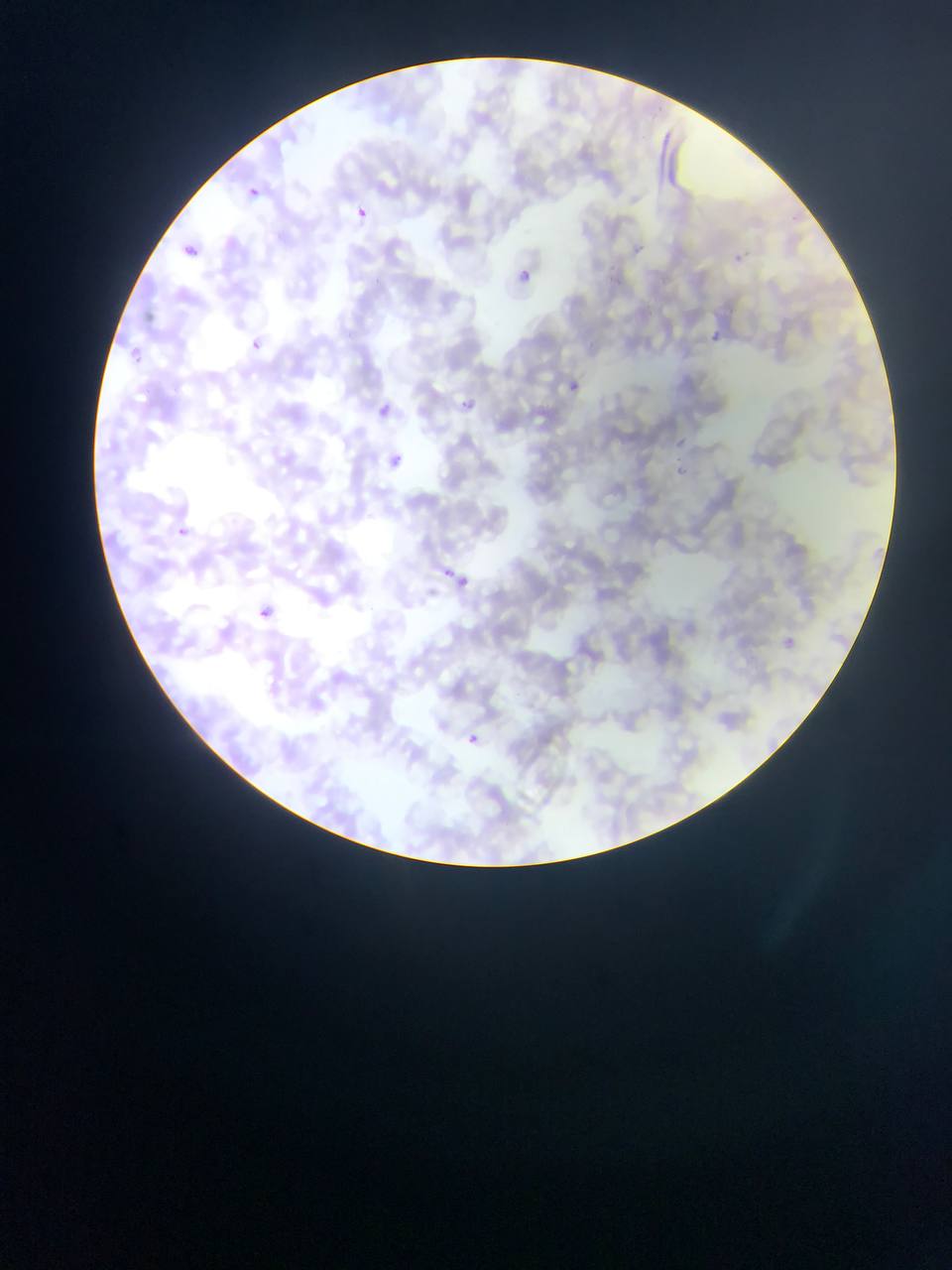 Approximate bounding boxes as [left, top, right, bottom] in pixels. Malaria parasite locations: [243, 186, 263, 203], [355, 207, 369, 220], [178, 241, 206, 258], [729, 250, 746, 267], [509, 262, 537, 290], [707, 327, 732, 352], [249, 339, 262, 352], [567, 380, 581, 394], [455, 395, 477, 414], [375, 401, 394, 419], [387, 450, 409, 476], [674, 466, 686, 477], [175, 523, 189, 539], [438, 565, 473, 595], [260, 609, 271, 619], [779, 635, 796, 650], [466, 732, 480, 745], [463, 733, 482, 750]. Photographed through a microscope with a mobile-phone camera. Image is 952×1270 pixels. One field of view. Thin blood film. Collected in Ghana.